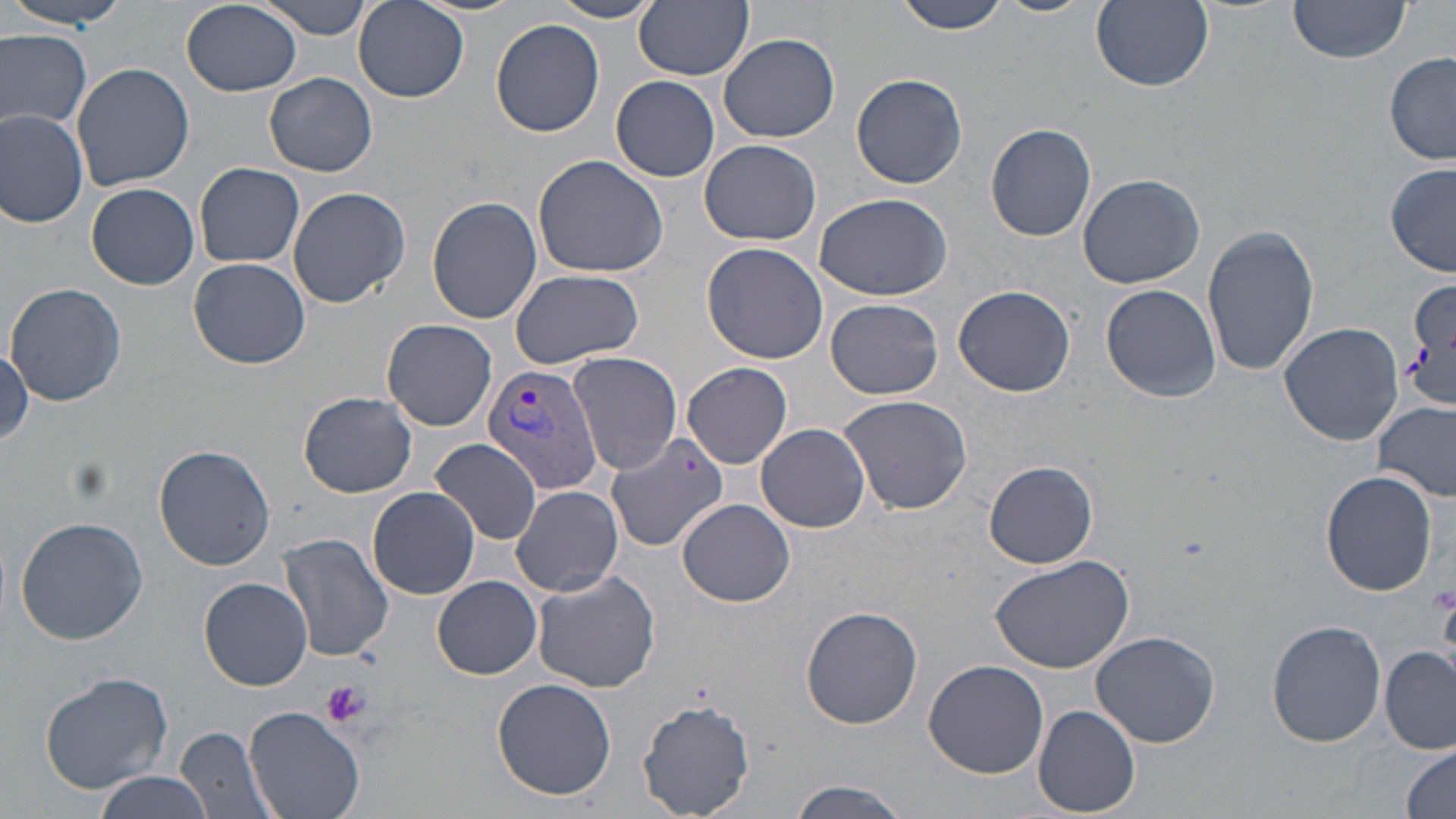 Approximate bounding boxes as named x1/y1/x2/y2 corners in pixels. Plasmodium vivax-infected red blood cell locations: (x1=481, y1=361, x2=606, y2=496). Platelet locations: (x1=1428, y1=579, x2=1456, y2=623), (x1=320, y1=678, x2=371, y2=727). Uninfected red blood cell locations: (x1=8, y1=0, x2=124, y2=29), (x1=257, y1=0, x2=376, y2=39), (x1=353, y1=0, x2=468, y2=102), (x1=897, y1=0, x2=1015, y2=37), (x1=992, y1=0, x2=1097, y2=17), (x1=1091, y1=0, x2=1214, y2=91), (x1=1287, y1=0, x2=1413, y2=62), (x1=181, y1=1, x2=302, y2=97), (x1=550, y1=1, x2=662, y2=24), (x1=635, y1=1, x2=754, y2=80), (x1=490, y1=19, x2=605, y2=136), (x1=0, y1=29, x2=92, y2=133), (x1=719, y1=33, x2=839, y2=143), (x1=1385, y1=53, x2=1455, y2=165), (x1=72, y1=62, x2=195, y2=190), (x1=265, y1=72, x2=378, y2=176), (x1=851, y1=72, x2=967, y2=188), (x1=612, y1=75, x2=721, y2=181), (x1=0, y1=109, x2=88, y2=228), (x1=985, y1=123, x2=1098, y2=242), (x1=698, y1=139, x2=822, y2=245), (x1=532, y1=154, x2=669, y2=280), (x1=195, y1=163, x2=303, y2=268), (x1=1386, y1=163, x2=1455, y2=278), (x1=1076, y1=172, x2=1205, y2=288), (x1=87, y1=183, x2=199, y2=289), (x1=288, y1=186, x2=410, y2=308), (x1=813, y1=193, x2=953, y2=302), (x1=427, y1=196, x2=542, y2=322), (x1=1202, y1=224, x2=1320, y2=378), (x1=699, y1=241, x2=830, y2=365), (x1=187, y1=256, x2=311, y2=369), (x1=509, y1=269, x2=644, y2=369), (x1=1402, y1=278, x2=1456, y2=409), (x1=7, y1=282, x2=125, y2=404), (x1=1101, y1=283, x2=1220, y2=402), (x1=953, y1=284, x2=1074, y2=396), (x1=826, y1=298, x2=945, y2=400), (x1=382, y1=319, x2=497, y2=431), (x1=1278, y1=321, x2=1403, y2=446), (x1=0, y1=347, x2=32, y2=449), (x1=569, y1=352, x2=682, y2=475), (x1=682, y1=362, x2=793, y2=468), (x1=299, y1=392, x2=418, y2=497), (x1=838, y1=393, x2=973, y2=517), (x1=1374, y1=400, x2=1455, y2=502), (x1=755, y1=423, x2=871, y2=532), (x1=605, y1=432, x2=731, y2=552), (x1=429, y1=438, x2=544, y2=545), (x1=154, y1=445, x2=274, y2=571), (x1=984, y1=461, x2=1098, y2=568), (x1=1321, y1=470, x2=1437, y2=595), (x1=512, y1=485, x2=624, y2=597), (x1=368, y1=486, x2=481, y2=600), (x1=677, y1=499, x2=797, y2=606), (x1=15, y1=516, x2=148, y2=645), (x1=277, y1=535, x2=394, y2=663), (x1=990, y1=553, x2=1135, y2=677), (x1=530, y1=570, x2=660, y2=693), (x1=433, y1=576, x2=542, y2=678), (x1=199, y1=577, x2=313, y2=691), (x1=802, y1=604, x2=923, y2=729), (x1=1266, y1=619, x2=1386, y2=748), (x1=1091, y1=630, x2=1220, y2=748), (x1=1382, y1=648, x2=1455, y2=753), (x1=924, y1=660, x2=1049, y2=778), (x1=40, y1=670, x2=173, y2=792), (x1=492, y1=676, x2=617, y2=801), (x1=638, y1=697, x2=756, y2=819), (x1=1033, y1=706, x2=1140, y2=816), (x1=244, y1=708, x2=366, y2=819), (x1=174, y1=725, x2=280, y2=819), (x1=1400, y1=744, x2=1456, y2=818), (x1=94, y1=774, x2=216, y2=819), (x1=785, y1=779, x2=915, y2=818). Slide-level diagnosis: Plasmodium vivax. Thin blood smear. One field of a larger specimen. Captured at 1000x magnification. May-Grünwald-Giemsa stain. Image is 1456×819 pixels. Light microscopy.